Describe the morphology of the red blood cells.
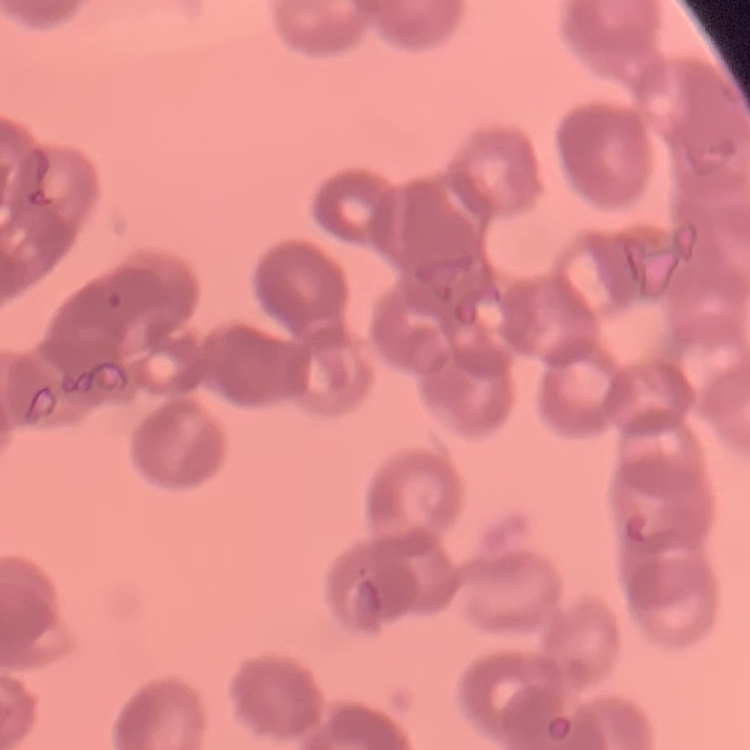
They show rouleaux formation.

stain = Field's or Giemsa
image type = one tile cut from a larger photomicrograph
preparation = thin peripheral smear